Give the extent of all Plasmodium falciparum-infected red blood cells.
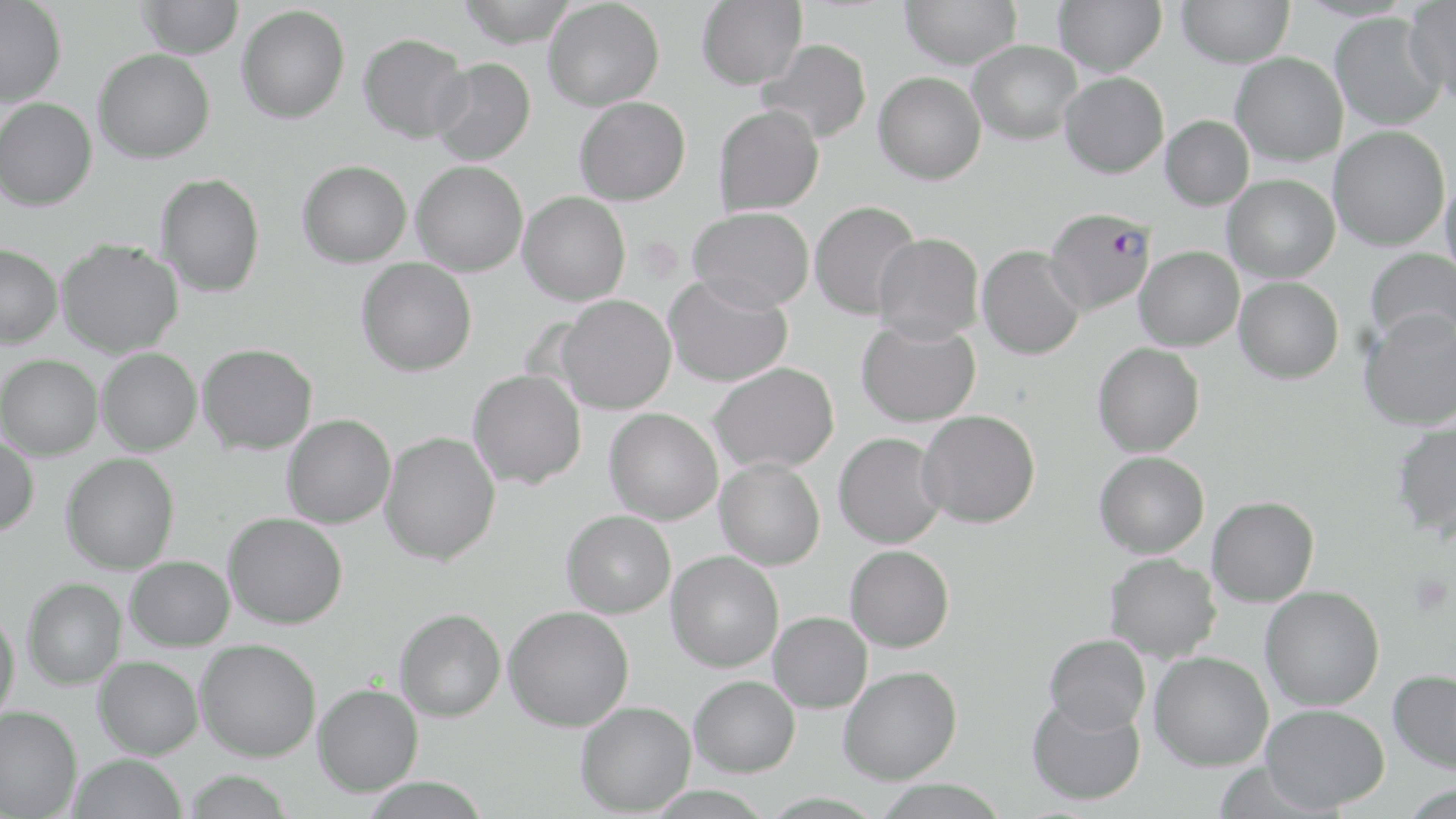

Approximate bounding boxes as [x1, y1, x2, y2] in pixels.
Plasmodium falciparum-infected red blood cells: [1043, 208, 1156, 315].

Uninfected red blood cell locations: [138, 0, 243, 59], [456, 0, 579, 47], [543, 0, 664, 111], [696, 0, 807, 90], [899, 0, 1022, 69], [1054, 0, 1166, 76], [1177, 0, 1294, 68], [1403, 0, 1456, 98], [0, 1, 66, 106], [237, 5, 350, 123], [1329, 12, 1445, 130], [358, 32, 471, 143], [758, 38, 872, 144], [967, 40, 1082, 145], [93, 49, 214, 163], [1231, 53, 1347, 165], [429, 57, 536, 165], [873, 71, 986, 185], [1060, 72, 1169, 178], [574, 96, 691, 205], [0, 98, 97, 210], [713, 104, 824, 215], [1160, 115, 1254, 211], [1329, 126, 1450, 251], [297, 160, 412, 268], [411, 161, 528, 277], [156, 173, 265, 297], [1223, 174, 1339, 282], [1440, 174, 1456, 282], [518, 191, 630, 305], [809, 200, 922, 321], [688, 206, 815, 312], [873, 233, 984, 343], [57, 239, 183, 357], [0, 244, 62, 348], [977, 245, 1085, 360], [1135, 246, 1244, 351], [1364, 248, 1456, 348], [356, 257, 477, 376], [663, 273, 793, 387], [1234, 277, 1344, 384], [556, 295, 676, 414], [1359, 308, 1456, 431], [856, 316, 981, 427], [198, 343, 317, 454], [1092, 343, 1204, 457], [97, 348, 201, 455], [1, 354, 102, 460], [709, 362, 838, 474], [468, 370, 586, 489], [604, 408, 723, 524], [917, 409, 1041, 528], [282, 414, 395, 528], [1390, 419, 1456, 538], [379, 431, 500, 565], [834, 432, 947, 548], [0, 436, 39, 536], [1094, 451, 1209, 558], [62, 453, 179, 574], [715, 459, 825, 570], [1207, 496, 1319, 606], [561, 510, 676, 617], [223, 512, 348, 628], [845, 545, 954, 652], [666, 551, 783, 672], [1104, 552, 1221, 662], [126, 556, 234, 651], [23, 578, 126, 689], [1260, 586, 1385, 711], [504, 606, 634, 731], [394, 608, 506, 721], [0, 610, 20, 722], [768, 612, 872, 713], [1044, 634, 1150, 734], [194, 639, 321, 761], [1148, 651, 1274, 771], [93, 656, 203, 759], [838, 665, 962, 784], [1387, 669, 1456, 773], [689, 675, 799, 776], [313, 684, 423, 796], [1026, 696, 1145, 805], [575, 701, 696, 815], [1260, 704, 1389, 812], [0, 705, 82, 818], [67, 753, 188, 819], [183, 771, 294, 819], [872, 779, 1009, 819]. Platelet locations: [1408, 574, 1453, 617]. Slide-level diagnosis: Plasmodium falciparum. Image is 1456×819 pixels. May-Grünwald-Giemsa-stained preparation. One field of a larger specimen. Optical microscopy. Captured at 1000x magnification. Thin blood smear.